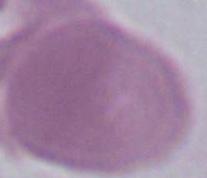

Summary:
  - Modality: photomicrograph
  - Magnification: 1000x
  - Identification: red blood cell